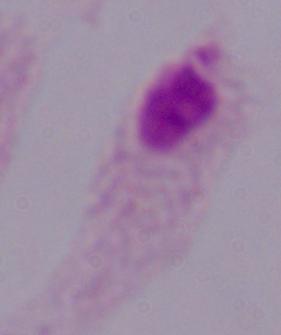
Micrograph. A trichomonad is shown. Captured at 1000x magnification.